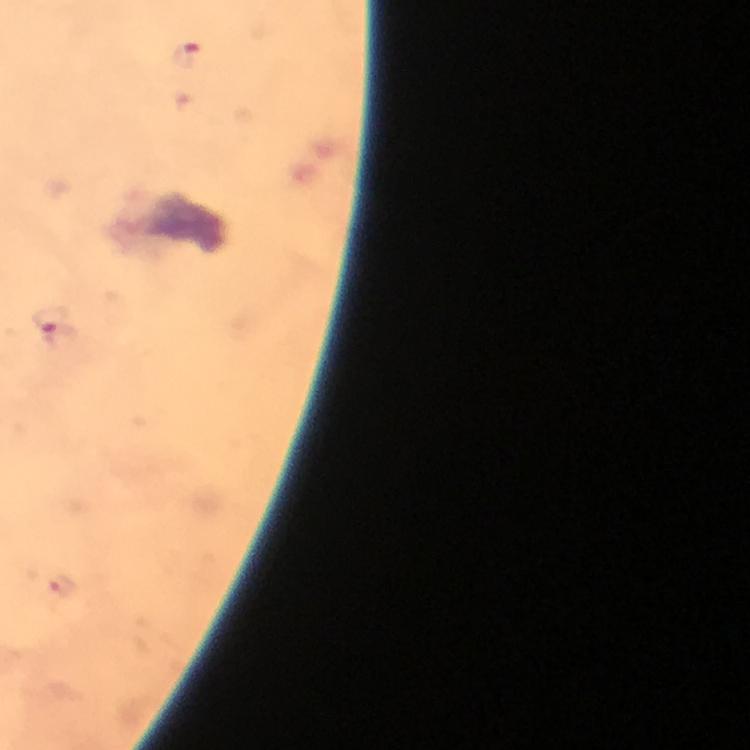
context = from a malaria diagnostic workup
magnification = 100x
preparation = thick blood film
image size = 750×750 pixels
stain = Giemsa
Plasmodium parasite locations = approximate centers as [x, y] in pixels: [187, 60], [57, 335], [61, 588]
cropped from = a single field of view
capture = smartphone camera through the microscope
immersion oil = applied